Assess this cell for malaria.
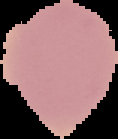
It is uninfected.

From a thin blood smear. The area outside the segmented cell region is set to black. Image is 118×139 pixels.